Point out Plasmodium parasites and leukocytes.
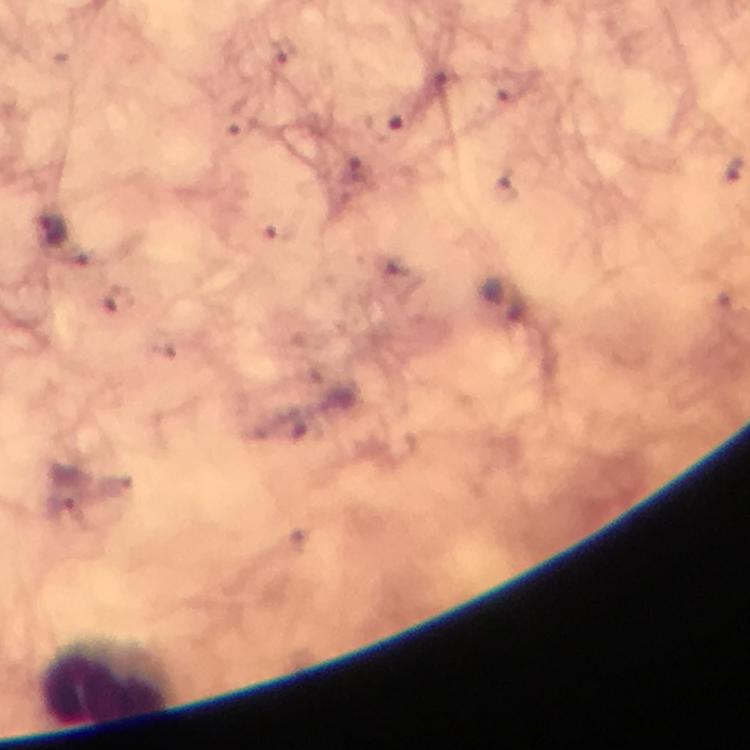
No Plasmodium parasites seen.
Approximate centers as [x, y] in pixels.
Leukocytes: [107, 686].

Cropped region of a single field of view. At 100x magnification. Image is 750×750 pixels. Thick blood smear. Photographed with a smartphone mounted on the microscope. From a diagnostic examination for malaria. Immersion oil was used. Giemsa-stained preparation.